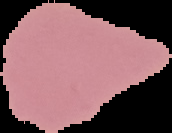

image size = 172×133 pixels
result = negative for malaria parasites
preparation = thin blood smear
image type = segmented cell region with the area outside set to black